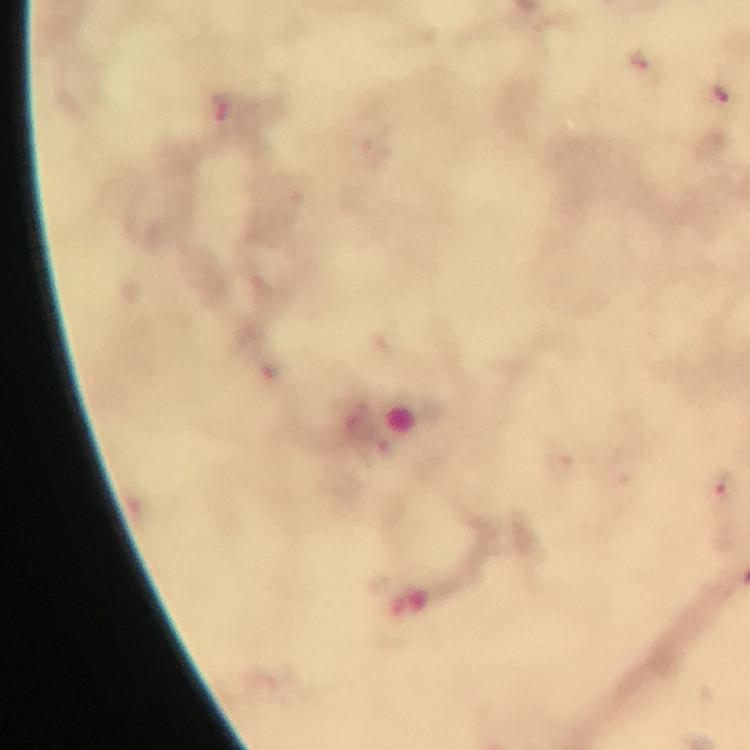 Approximate centers as [x, y] in pixels. Plasmodium parasite locations: [725, 488]. Thick smear. Image is 750×750 pixels. From a malaria diagnostic workup. Giemsa stain. Immersion oil applied. At 100x magnification. Photographed through the microscope with a smartphone camera. A crop from one field of view.